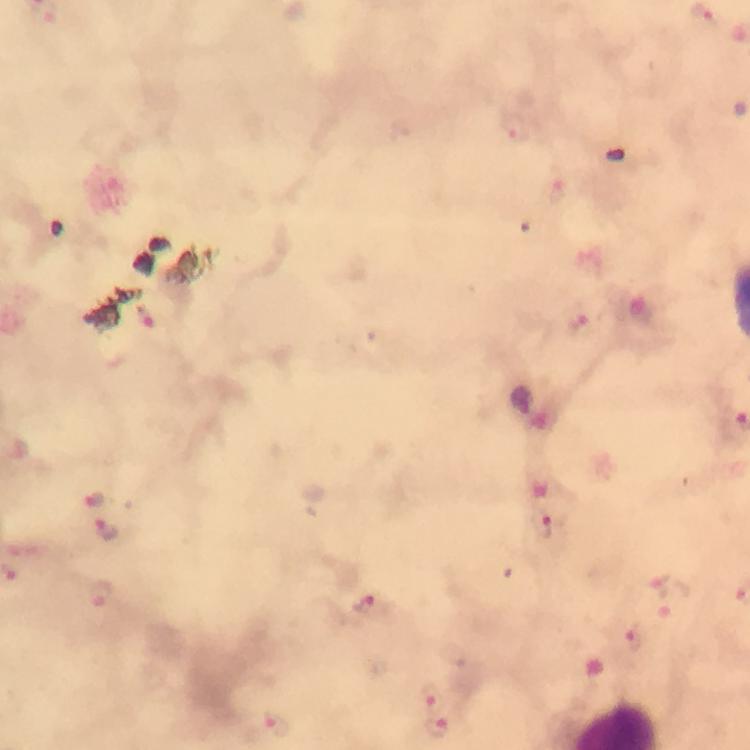 Approximate centers as [x, y] in pixels. Malaria parasite locations: [515, 128], [559, 195], [144, 316], [576, 325], [94, 499], [544, 528], [110, 530], [658, 577], [101, 597], [667, 608], [371, 609], [634, 638], [431, 691], [273, 724], [438, 729]. Immersion oil was used. Giemsa stain. Cropped region of a single field of view. From a diagnostic examination for malaria. Image is 750×750 pixels. 100x magnification. Thick smear. Photographed through the microscope with a smartphone camera.